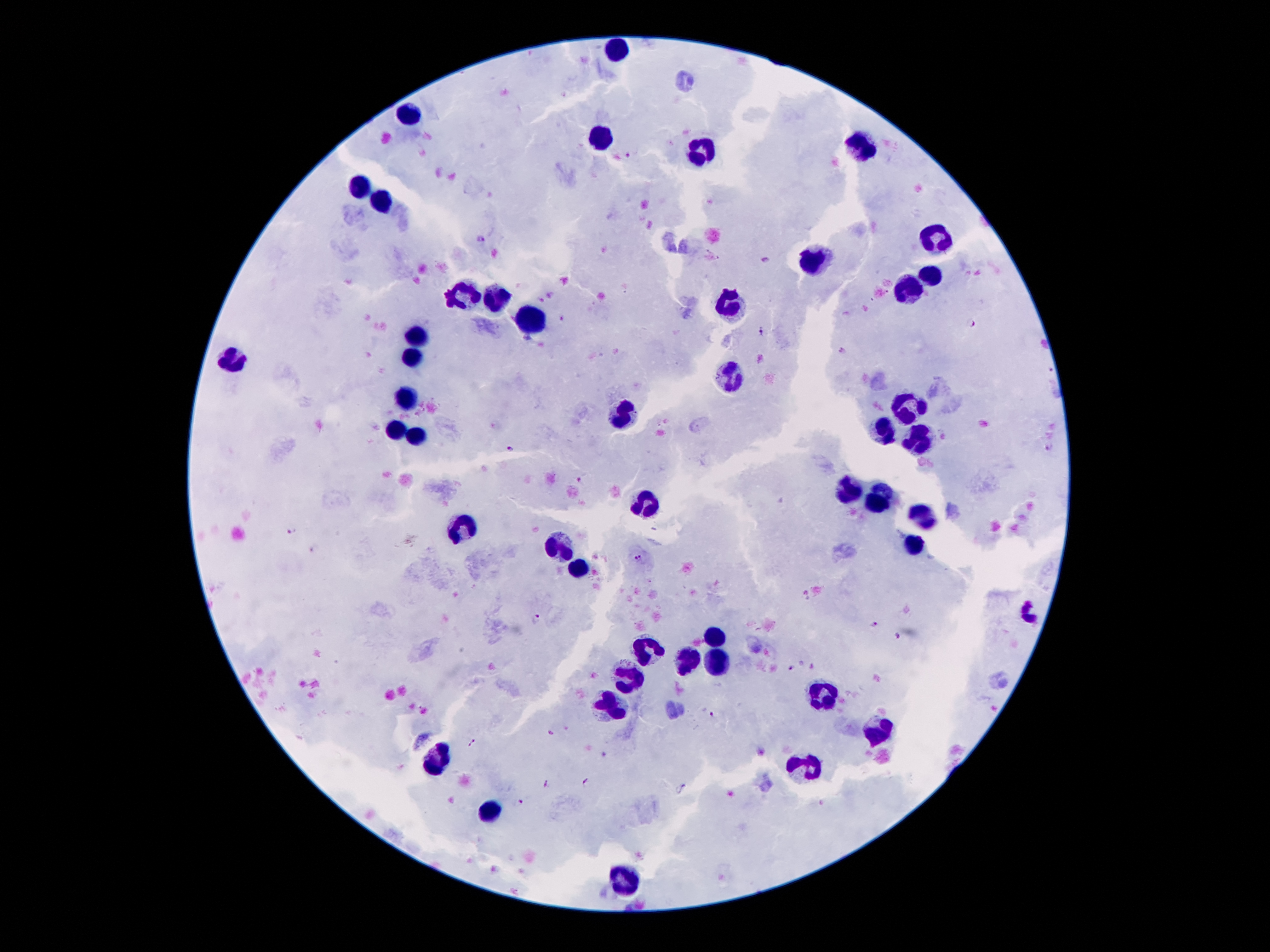
Approximate centers as {x, y} in pixels.
Summary:
  - Leukocyte locations: {615, 51}, {409, 110}, {599, 140}, {861, 147}, {702, 152}, {357, 186}, {384, 204}, {935, 240}, {811, 261}, {927, 277}, {906, 288}, {459, 299}, {491, 301}, {729, 306}, {527, 320}, {420, 335}, {413, 354}, {234, 358}, {729, 374}, {407, 399}, {908, 408}, {618, 415}, {883, 429}, {397, 431}, {418, 433}, {919, 435}, {844, 492}, {877, 495}, {647, 502}, {922, 517}, {463, 529}, {913, 544}, {559, 545}, {581, 567}, {1029, 610}, {717, 636}, {652, 649}, {688, 656}, {720, 663}, {627, 681}, {824, 695}, {609, 708}, {877, 729}, {438, 761}, {801, 767}, {491, 811}, {624, 879}
  - Malaria parasite locations: {629, 153}, {480, 240}, {765, 260}, {552, 295}, {540, 299}, {562, 320}, {969, 323}, {761, 332}, {528, 341}, {841, 352}, {1050, 444}, {512, 449}, {585, 478}, {293, 528}, {315, 548}, {638, 558}, {535, 619}, {873, 625}, {897, 638}, {813, 665}, {792, 667}, {988, 709}, {712, 715}, {550, 732}, {472, 742}, {547, 783}, {588, 783}, {522, 801}
  - Magnification: 100x
  - Preparation: thick blood film
  - Patient malaria status: positive for Plasmodium falciparum
  - Capture: smartphone camera through the microscope eyepiece
  - Stain: Giemsa
  - Image size: 1270×952 pixels
  - Field of view: one from this slide